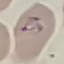 Result: malaria parasites identified. Cell patch, automatically extracted from a larger field of view and resized to 64 × 64 pixels. Thin smear of blood. Acquired by smartphone through the microscope eyepiece. Giemsa-stained preparation.